Classify this cell by malaria status.
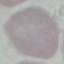

Uninfected.

stain = Giemsa
capture = smartphone through the microscope eyepiece
image type = automatically extracted cell patch, resized to 64 × 64 pixels
preparation = thin blood film